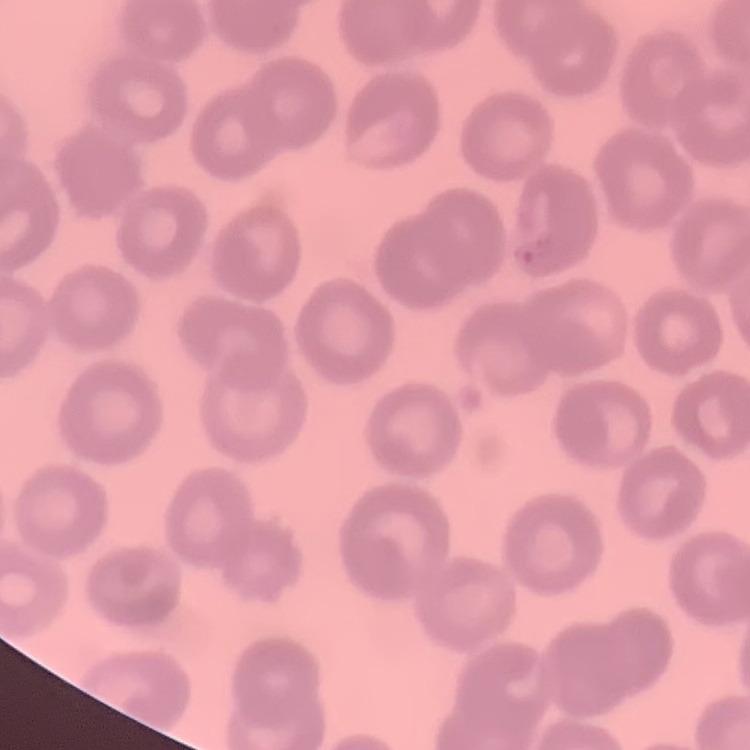

red_blood_cell_morphology: no rouleaux formation
preparation: thin peripheral smear
image_type: one tile cut from a larger photomicrograph
stain: Field's or Giemsa